Report the malaria status of this cell.
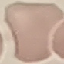
Uninfected.

Cell patch, automatically extracted from a larger field of view and resized to 64 × 64 pixels. Thin blood smear. Photographed with a smartphone camera at the microscope eyepiece. Giemsa-stained preparation.